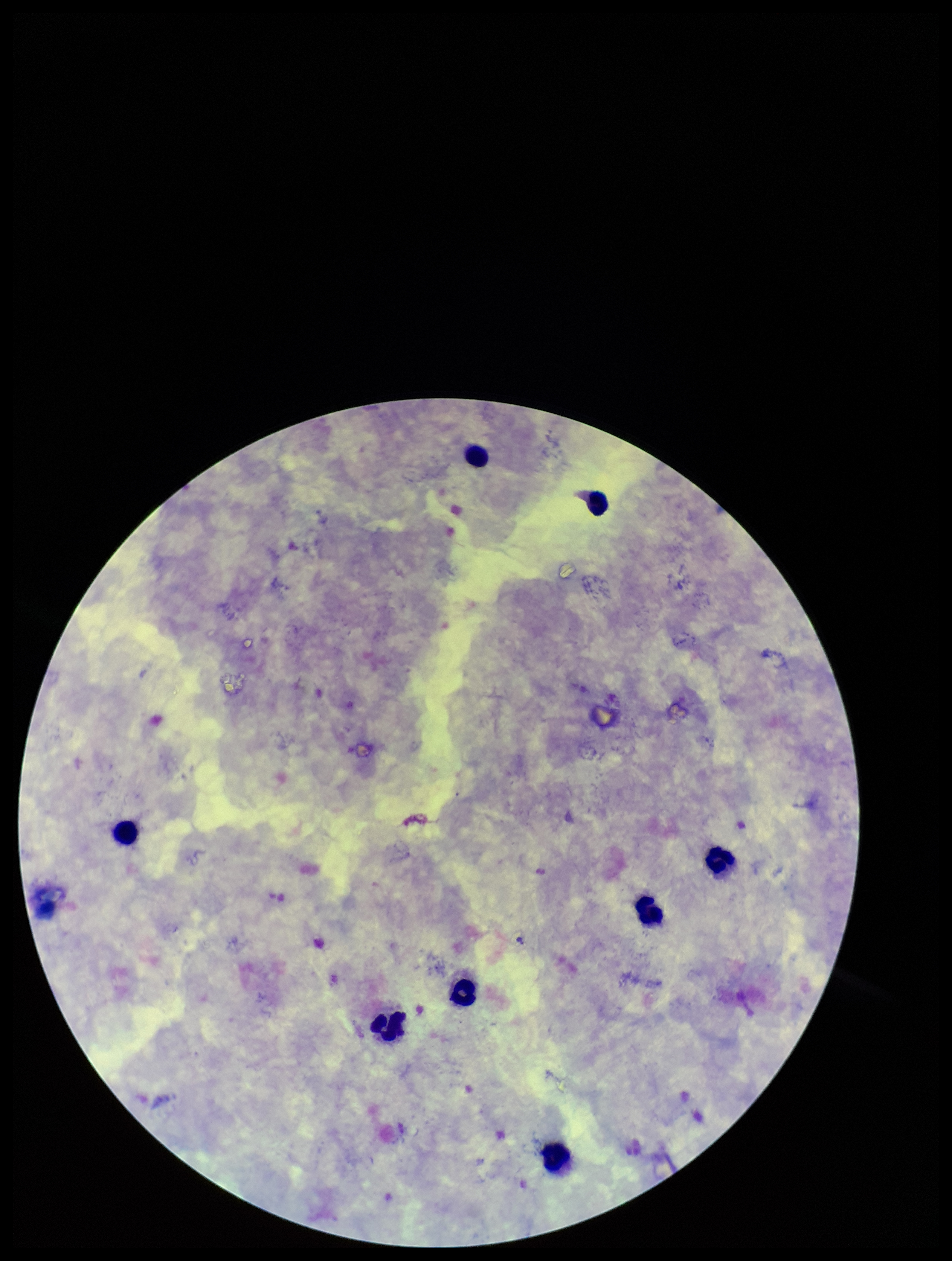
Summary:
  - Parasite count: 0
  - Plasmodium parasites: none identified
  - Image size: 952×1261 pixels
  - Preparation: thick blood smear
  - Stain: Giemsa
  - Field of view: one from this slide
  - Leukocyte count: 8
  - Capture: smartphone photograph through the microscope eyepiece
  - Patient malaria status: negative